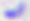
Summary:
  - Modality: photomicrograph
  - Identification: Toxoplasma gondii
  - Magnification: 400x